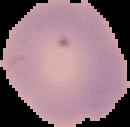
image type = cell region segmented out of the field of view; surrounding area masked to black
image size = 130×127 pixels
result = no Plasmodium parasites seen
preparation = thin blood smear